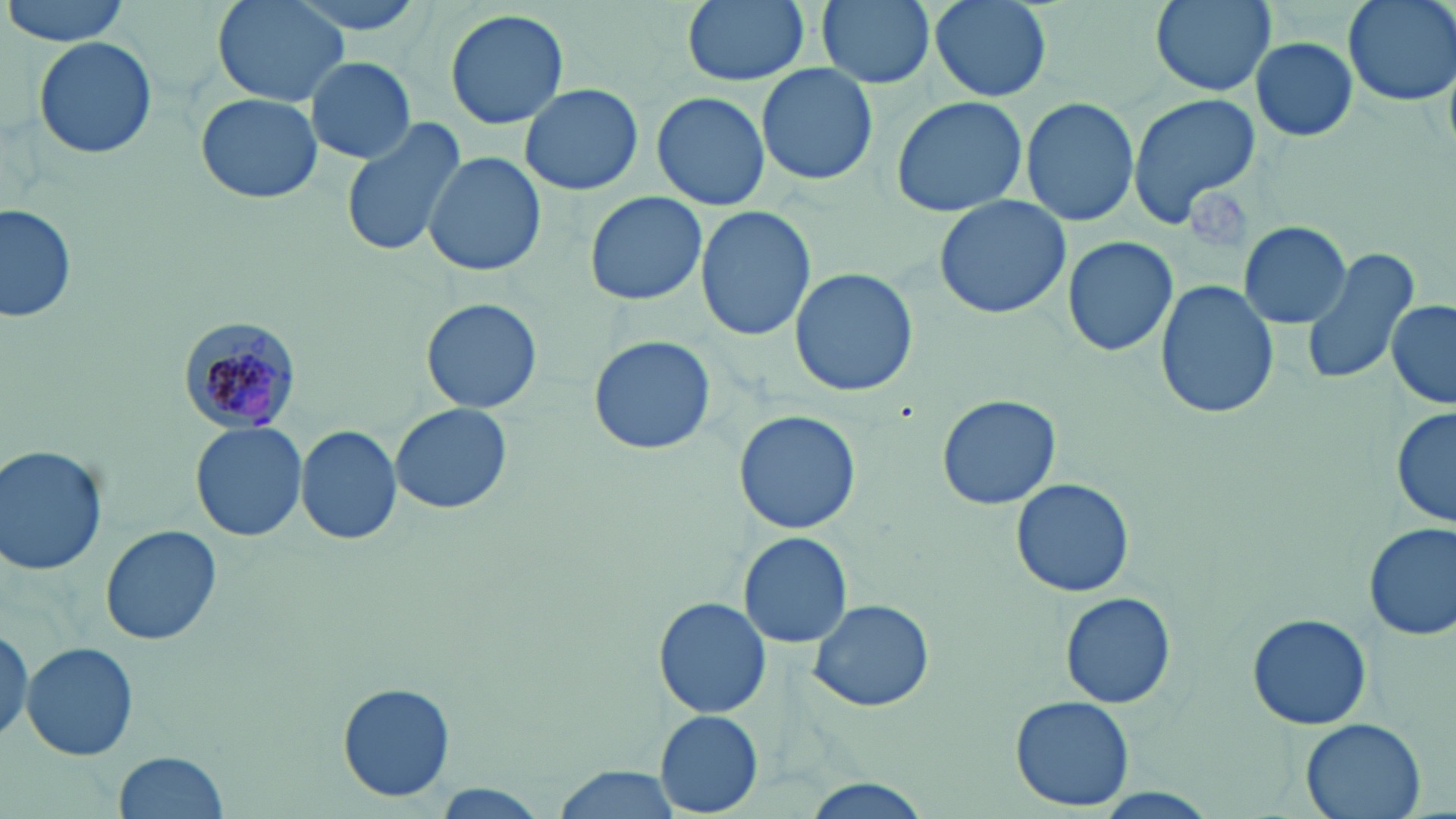
Summary:
  - Coordinate format: approximate bounding boxes as named x1/y1/x2/y2 corners in pixels
  - Platelet locations: (x1=1187, y1=185, x2=1250, y2=245)
  - Uninfected red blood cell locations: (x1=4, y1=0, x2=132, y2=46), (x1=211, y1=0, x2=350, y2=107), (x1=280, y1=0, x2=433, y2=37), (x1=681, y1=0, x2=809, y2=87), (x1=816, y1=0, x2=935, y2=89), (x1=926, y1=0, x2=1055, y2=103), (x1=1144, y1=0, x2=1280, y2=98), (x1=1341, y1=0, x2=1455, y2=106), (x1=444, y1=7, x2=569, y2=131), (x1=33, y1=34, x2=157, y2=161), (x1=1250, y1=38, x2=1358, y2=141), (x1=305, y1=56, x2=414, y2=164), (x1=754, y1=64, x2=879, y2=185), (x1=520, y1=81, x2=643, y2=196), (x1=651, y1=90, x2=771, y2=210), (x1=194, y1=92, x2=323, y2=204), (x1=1127, y1=92, x2=1263, y2=228), (x1=891, y1=96, x2=1028, y2=219), (x1=1021, y1=98, x2=1138, y2=226), (x1=338, y1=113, x2=466, y2=261), (x1=423, y1=151, x2=547, y2=278), (x1=584, y1=191, x2=707, y2=306), (x1=933, y1=194, x2=1070, y2=320), (x1=0, y1=201, x2=75, y2=323), (x1=695, y1=205, x2=816, y2=342), (x1=1240, y1=220, x2=1351, y2=328), (x1=1061, y1=236, x2=1178, y2=357), (x1=1301, y1=245, x2=1420, y2=387), (x1=789, y1=267, x2=918, y2=397), (x1=1154, y1=278, x2=1279, y2=421), (x1=421, y1=297, x2=544, y2=414), (x1=1387, y1=299, x2=1455, y2=411), (x1=588, y1=334, x2=716, y2=458), (x1=935, y1=393, x2=1061, y2=510), (x1=389, y1=402, x2=513, y2=515), (x1=1391, y1=407, x2=1454, y2=531), (x1=733, y1=409, x2=861, y2=535), (x1=189, y1=421, x2=305, y2=541), (x1=298, y1=427, x2=402, y2=544), (x1=0, y1=445, x2=108, y2=575), (x1=1011, y1=478, x2=1135, y2=597), (x1=1362, y1=523, x2=1456, y2=643), (x1=100, y1=525, x2=222, y2=645), (x1=740, y1=531, x2=852, y2=648), (x1=1061, y1=592, x2=1176, y2=709), (x1=652, y1=598, x2=774, y2=719), (x1=808, y1=598, x2=933, y2=712), (x1=1246, y1=612, x2=1372, y2=729), (x1=23, y1=641, x2=138, y2=761), (x1=336, y1=682, x2=456, y2=805), (x1=1011, y1=696, x2=1135, y2=811), (x1=654, y1=710, x2=764, y2=815), (x1=1301, y1=718, x2=1428, y2=819), (x1=114, y1=751, x2=228, y2=818), (x1=547, y1=765, x2=680, y2=819), (x1=797, y1=782, x2=931, y2=818), (x1=429, y1=784, x2=551, y2=815)
  - Plasmodium malariae-infected red blood cell locations: (x1=177, y1=313, x2=303, y2=436)
  - Slide-level diagnosis: Plasmodium malariae
  - Field of view: single
  - Magnification: 1000x
  - Stain: May-Grünwald-Giemsa
  - Preparation: thin blood smear
  - Image size: 1456×819 pixels
  - Modality: light microscopy